Point out each malaria parasite.
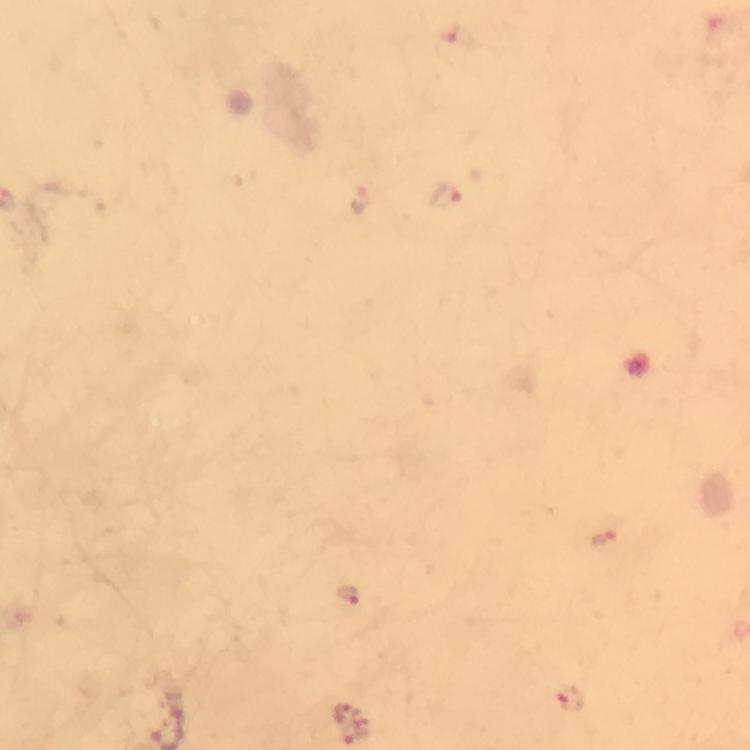
Approximate centers as (x, y) in pixels.
Malaria parasites: (448, 197), (361, 201), (602, 537), (350, 596), (570, 699), (344, 711), (355, 734).

Immersion oil applied. Image is 750×750 pixels. 100x magnification. Cropped region of a single field of view. Giemsa stain. Thick blood film. From a diagnostic examination for malaria. Photographed with a smartphone mounted on the microscope.